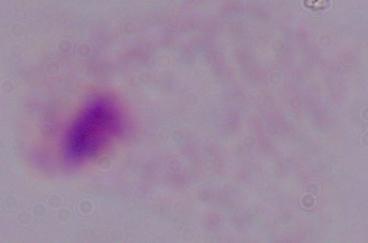
Summary:
  - Identification: trichomonad
  - Magnification: 1000x
  - Modality: micrograph